Classify this cell by malaria status.
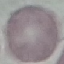

It is uninfected.

Summary:
  - Capture: smartphone camera at the microscope eyepiece
  - Stain: Giemsa
  - Image type: cell patch, automatically extracted from a larger field of view and resized to 64 × 64 pixels
  - Preparation: thin blood smear